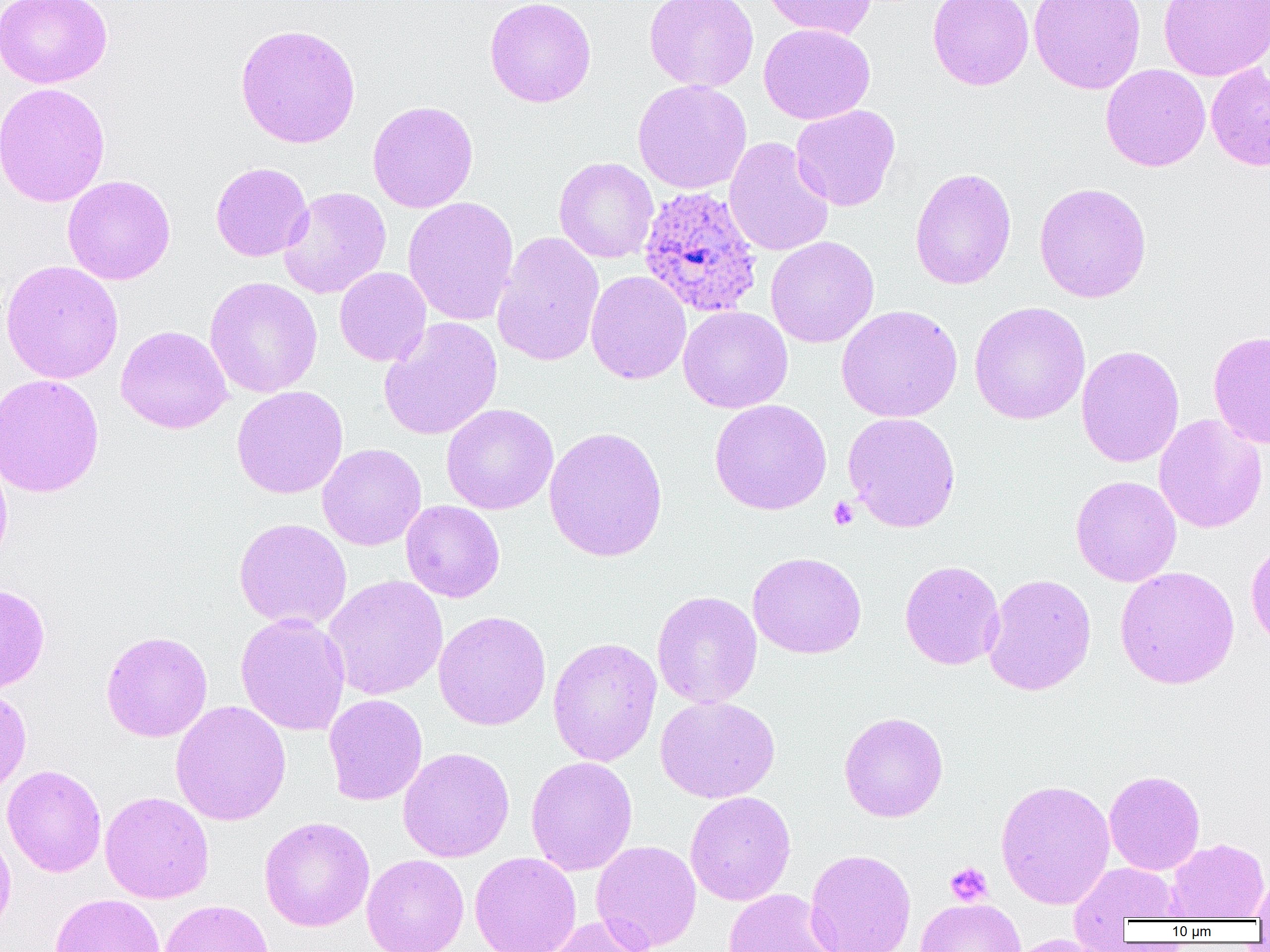 Approximate bounding boxes as (x1, y1, x2, y2) in pixels. Platelet locations: (828, 496, 859, 530), (945, 862, 993, 906). Plasmodium ovale-infected red blood cell locations: (638, 185, 764, 318). Uninfected red blood cell locations: (0, 0, 112, 89), (484, 0, 597, 108), (643, 0, 759, 92), (760, 0, 876, 39), (927, 0, 1034, 90), (1028, 0, 1146, 94), (1158, 0, 1270, 81), (758, 22, 875, 125), (235, 23, 361, 149), (1205, 63, 1270, 172), (1100, 64, 1211, 172), (632, 79, 752, 194), (0, 81, 110, 207), (367, 100, 478, 213), (790, 105, 901, 211), (723, 136, 834, 257), (554, 157, 659, 263), (210, 162, 313, 262), (909, 167, 1017, 290), (62, 175, 176, 285), (1034, 182, 1152, 303), (278, 186, 392, 298), (402, 196, 519, 326), (492, 231, 605, 367), (766, 237, 879, 348), (1, 259, 123, 384), (334, 267, 432, 366), (585, 270, 691, 384), (203, 276, 323, 398), (969, 301, 1091, 425), (836, 304, 963, 423), (678, 305, 793, 413), (378, 317, 503, 441), (116, 325, 232, 434), (1208, 330, 1270, 448), (1076, 345, 1184, 468), (0, 373, 105, 498), (231, 386, 348, 499), (709, 399, 832, 515), (441, 403, 558, 515), (843, 411, 961, 533), (1153, 414, 1267, 533), (543, 426, 668, 562), (317, 443, 427, 550), (0, 447, 13, 571), (1071, 475, 1182, 586), (400, 500, 505, 602), (234, 517, 352, 630), (1246, 538, 1270, 653), (748, 551, 867, 659), (899, 560, 1005, 670), (1114, 566, 1239, 689), (982, 573, 1096, 696), (324, 575, 448, 700), (0, 583, 50, 694), (652, 590, 762, 708), (433, 610, 552, 731), (235, 612, 350, 736), (101, 630, 213, 742), (547, 637, 662, 767), (0, 686, 32, 796), (324, 694, 427, 806), (654, 695, 780, 803), (170, 700, 291, 826), (839, 711, 949, 822), (398, 746, 515, 863), (525, 756, 638, 876), (2, 764, 107, 878), (1104, 770, 1205, 875), (995, 778, 1116, 910), (100, 791, 214, 903), (685, 791, 796, 906), (258, 816, 375, 931), (0, 823, 16, 939), (1166, 838, 1269, 920), (591, 840, 702, 951), (805, 849, 917, 952), (469, 851, 582, 952), (361, 854, 469, 952), (1069, 863, 1182, 930), (1251, 873, 1270, 921), (722, 888, 841, 952), (50, 893, 166, 952), (915, 898, 1026, 952), (157, 899, 273, 952), (544, 915, 656, 952), (1001, 934, 1117, 952). Slide-level diagnosis: Plasmodium ovale. Thin blood film. 1000x magnification. Image is 1270×952 pixels. Single field of view. Optical microscopy.